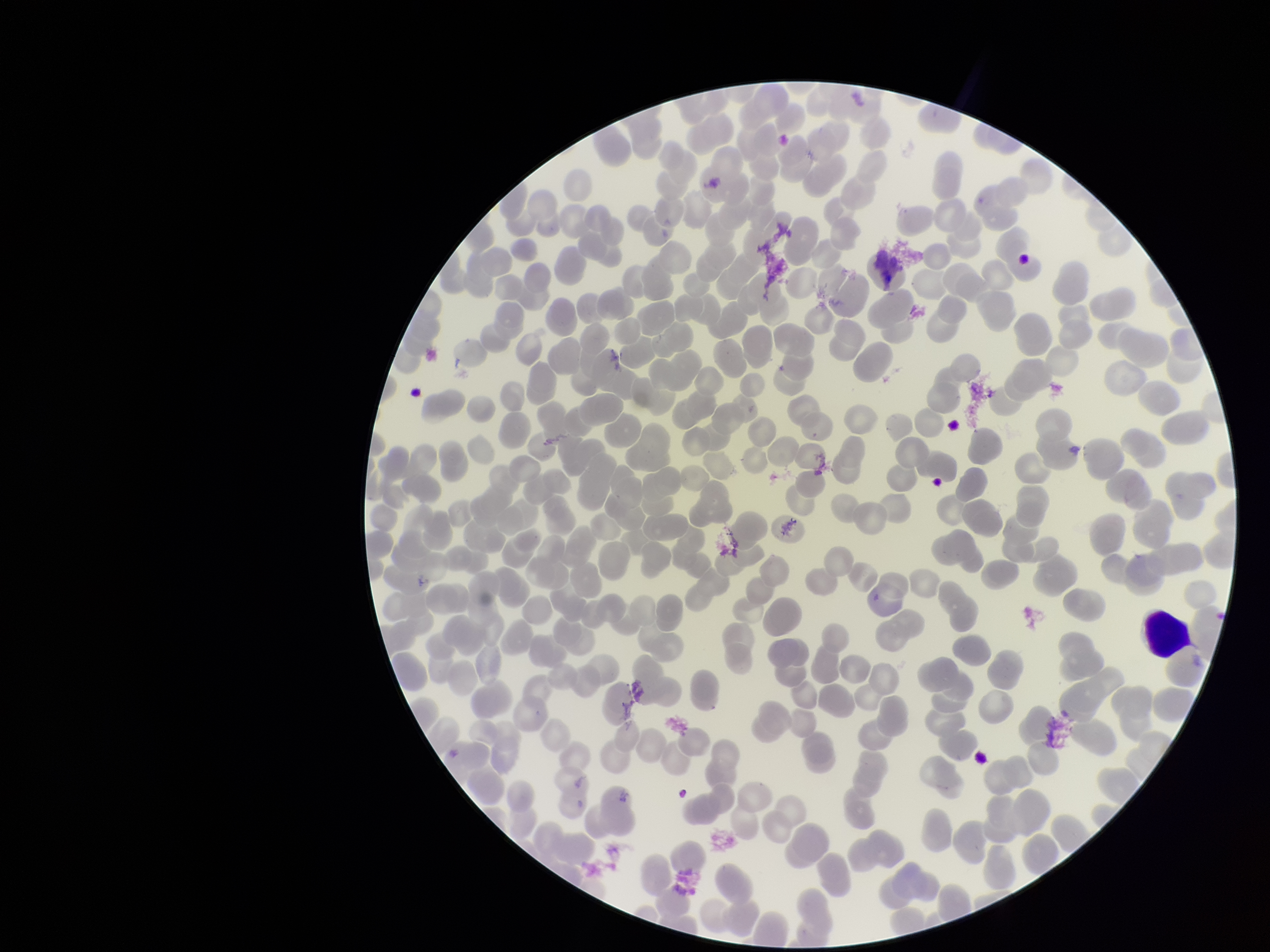

Single field of view. Patient malaria status: positive. Giemsa stain. Species reported for this patient: Plasmodium falciparum. Image is 1270×952 pixels. Photographed through the microscope eyepiece with a smartphone camera. Parasitized red blood cell count: 0. Red blood cell count: 252. Preparation: thin smear. Parasitized red blood cells: none identified.